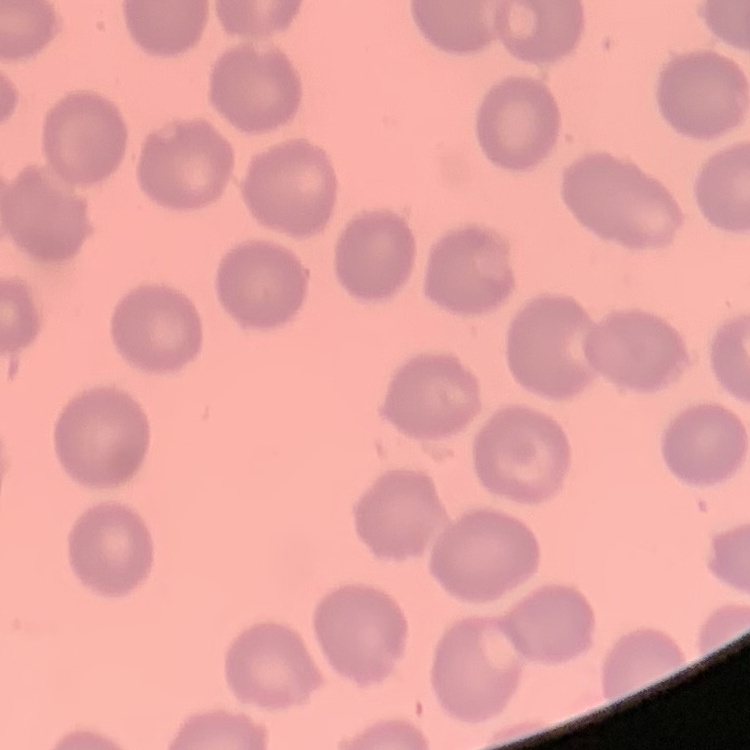
erythrocyte morphology = no rouleaux formation
image type = square crop of a larger photomicrograph
stain = Field's or Giemsa
preparation = thin peripheral smear